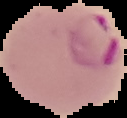

The area outside the segmented cell region is set to black. From a thin blood film. Result: Plasmodium parasites identified. Image is 127×118 pixels.